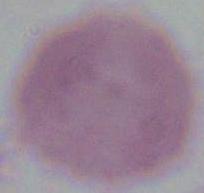
Summary:
  - Modality: micrograph
  - Magnification: 1000x
  - Identification: red blood cell